Assess the morphology of the erythrocytes.
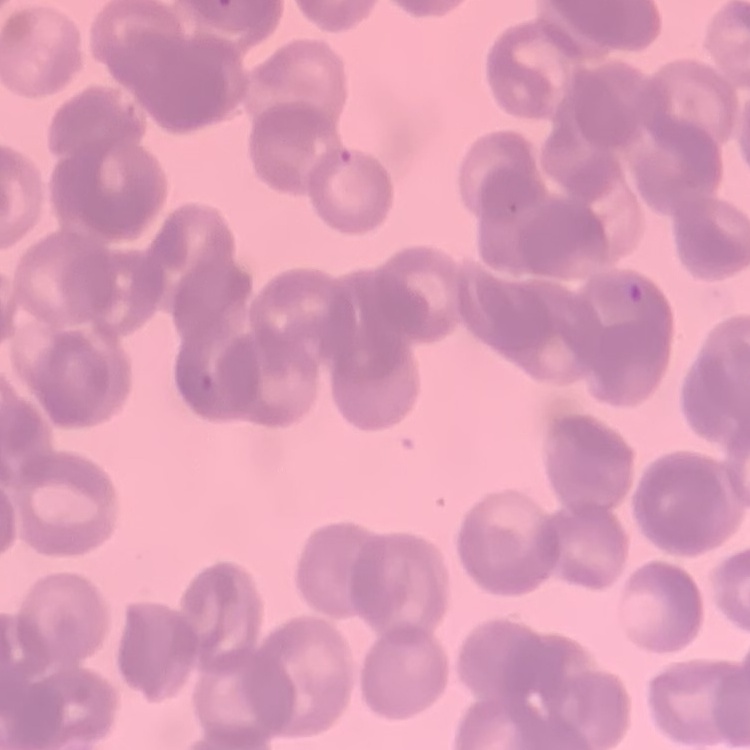
They show rouleaux formation.

Summary:
  - Preparation: thin blood film
  - Stain: Field's or Giemsa
  - Image type: one tile cut from a larger photomicrograph